Comment on the morphology of the erythrocytes.
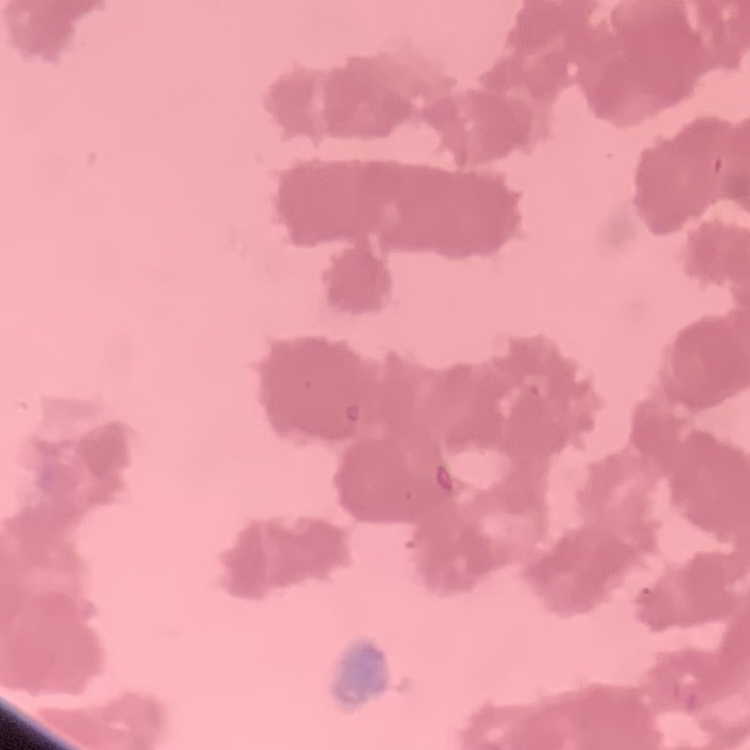

They show rouleaux formation.

One tile cut from a larger photomicrograph. Thin blood film. Field's or Giemsa stain.